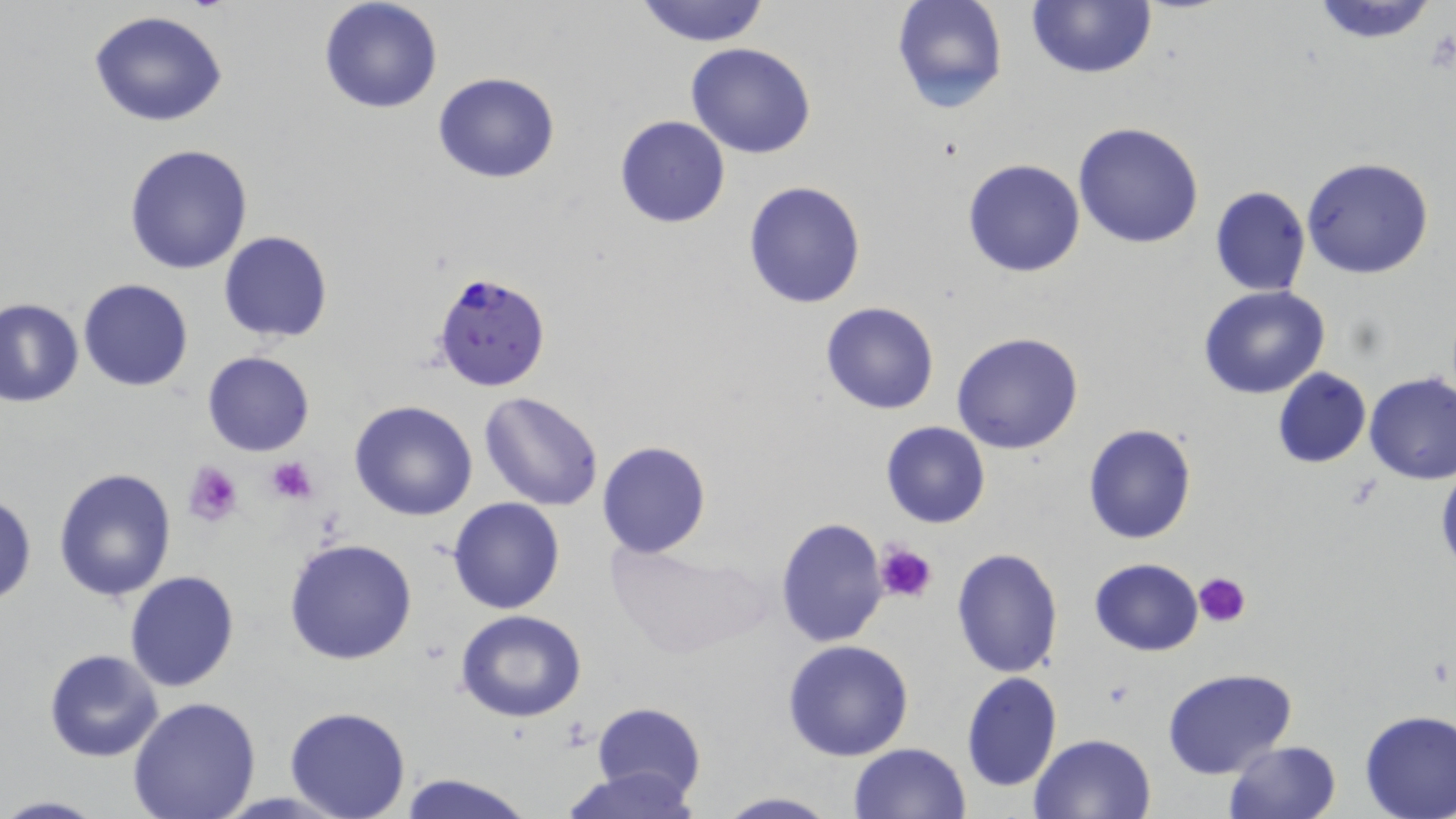
Summary:
  - Coordinate format: approximate bounding boxes as (x1,y1)-(x2,y2) corner pairs in pixels
  - Uninfected red blood cell locations: (319,0)-(444,114), (634,0)-(772,47), (893,0)-(1008,116), (1308,0)-(1442,45), (1027,1)-(1156,77), (88,10)-(230,127), (685,42)-(817,159), (432,71)-(560,184), (614,114)-(731,230), (1073,123)-(1204,249), (124,144)-(253,274), (1302,157)-(1435,279), (962,159)-(1085,277), (742,180)-(868,309), (1209,185)-(1310,297), (218,231)-(335,343), (79,279)-(192,391), (1200,286)-(1330,399), (0,297)-(84,408), (821,302)-(939,415), (950,332)-(1084,455), (203,351)-(315,457), (1272,367)-(1372,468), (1364,372)-(1456,486), (477,391)-(605,511), (350,400)-(477,520), (880,420)-(991,530), (1082,423)-(1198,545), (596,440)-(711,559), (1435,462)-(1456,580), (53,467)-(175,601), (0,491)-(36,605), (447,497)-(566,615), (774,517)-(890,648), (285,537)-(419,666), (605,540)-(768,661), (950,549)-(1064,679), (1089,557)-(1205,655), (125,570)-(240,692), (456,610)-(587,723), (782,639)-(915,761), (45,649)-(164,762), (1161,667)-(1299,780), (960,672)-(1062,793), (127,697)-(261,818), (593,702)-(706,806), (285,707)-(411,819), (1358,709)-(1456,819), (1028,732)-(1158,819), (1223,739)-(1343,819), (848,742)-(970,819), (564,764)-(701,819), (396,771)-(533,819), (713,792)-(838,819), (0,795)-(108,818)
  - Platelet locations: (265,455)-(319,504), (183,462)-(245,527), (876,540)-(939,605), (1193,572)-(1250,628)
  - Plasmodium falciparum-infected red blood cell locations: (431,271)-(552,394)
  - Slide-level diagnosis: Plasmodium falciparum
  - Preparation: thin blood smear
  - Modality: light microscopy
  - Field of view: one of a larger specimen
  - Image size: 1456×819 pixels
  - Stain: May-Grünwald-Giemsa
  - Magnification: 1000x